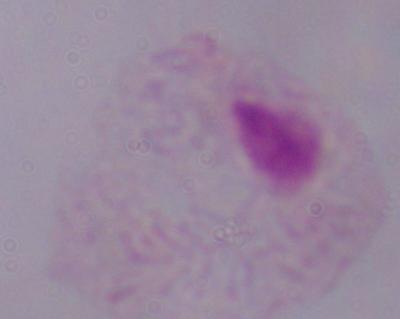

modality: micrograph
magnification: 1000x
identification: trichomonad